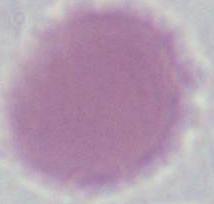
modality: photomicrograph
magnification: 1000x
identification: erythrocyte